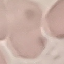 Malaria status: uninfected. Acquired by smartphone through the microscope eyepiece. Giemsa stain. Thin smear of blood. Automatically extracted cell patch, resized to 64 × 64 pixels.